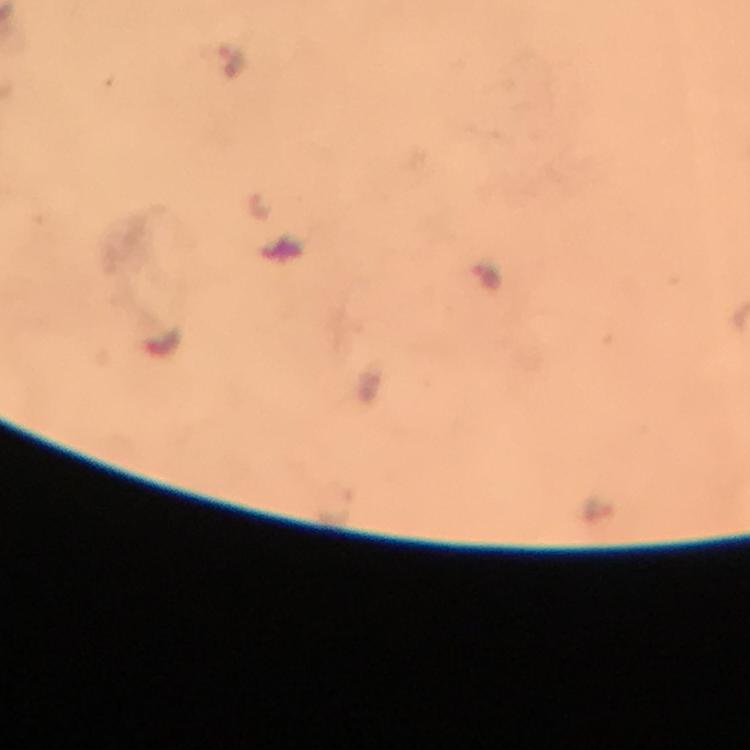

Approximate centers as (x, y) in pixels. Malaria parasite locations: (230, 60), (488, 280). Photographed through the microscope with a smartphone camera. 100x magnification. Giemsa stain. Thick blood film. Image is 750×750 pixels. From a diagnostic examination for malaria. A crop from one field of view. Immersion oil applied.